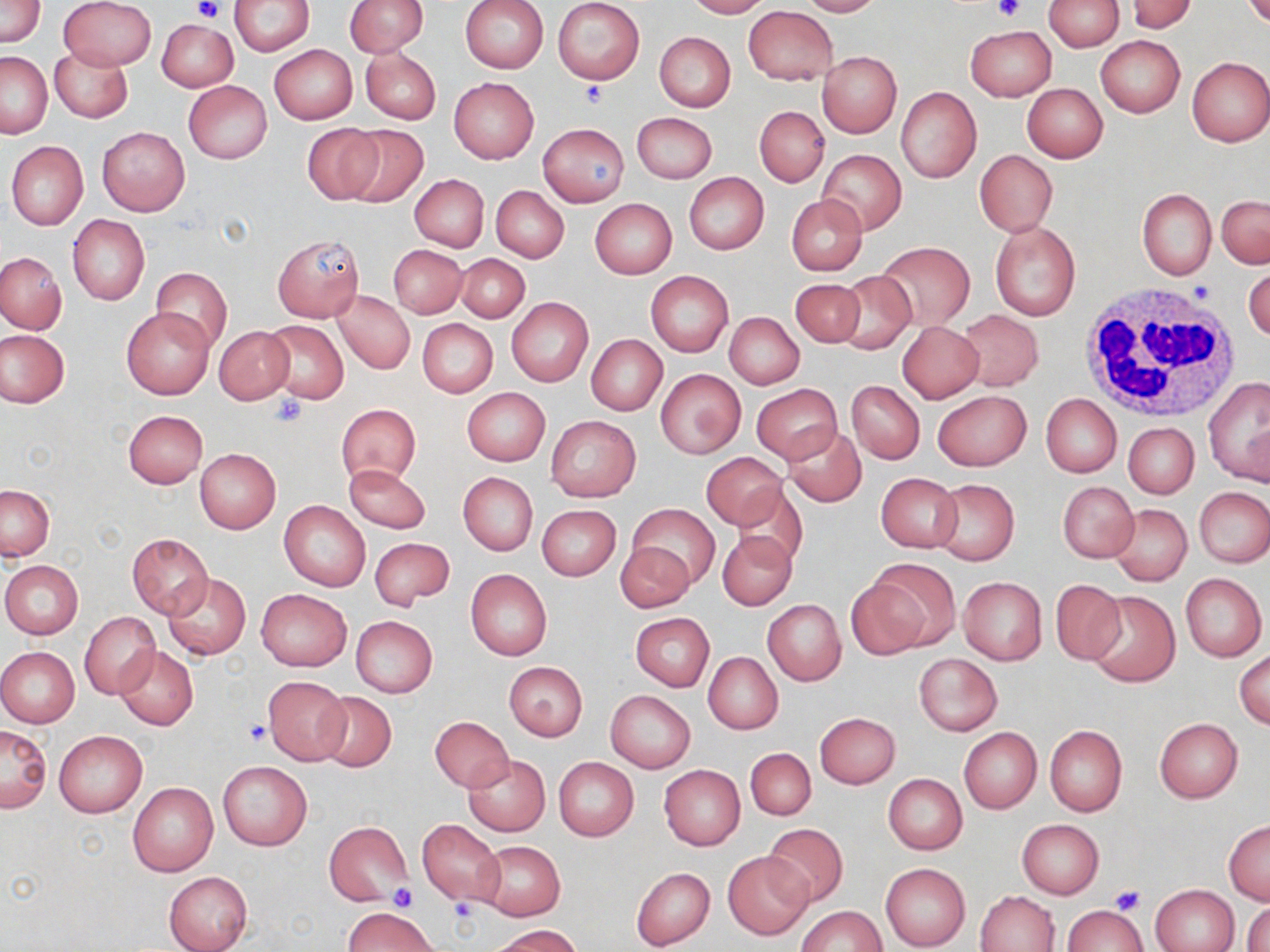
slide_level_diagnosis: negative for blood parasites
field_of_view: one of a larger specimen
uninfected_red_blood_cell_locations: 'approximate bounding boxes as [x1, y1, x2, y2] in pixels: [0, 0, 45, 48], [61, 0, 155, 69], [229, 0, 316, 56], [345, 0, 428, 56], [459, 0, 548, 73], [553, 0, 645, 84], [685, 0, 769, 18], [795, 0, 881, 17], [1043, 0, 1124, 50], [1126, 0, 1197, 34], [1244, 0, 1270, 29], [744, 6, 837, 85], [156, 18, 238, 92], [965, 26, 1056, 100], [653, 32, 735, 112], [1096, 36, 1184, 117], [640, 38, 719, 184], [270, 45, 357, 124], [51, 47, 133, 123], [360, 48, 440, 123], [818, 51, 901, 137], [1, 52, 51, 138], [1186, 57, 1270, 147], [449, 77, 539, 164], [183, 81, 271, 164], [1022, 83, 1108, 162], [896, 86, 982, 183], [755, 106, 828, 187], [632, 112, 716, 184], [301, 123, 386, 203], [340, 123, 429, 208], [537, 123, 630, 206], [98, 126, 190, 216], [6, 141, 89, 230], [817, 150, 906, 233], [974, 150, 1057, 237], [684, 173, 769, 255], [409, 174, 488, 253], [491, 186, 568, 263], [1137, 189, 1216, 279], [786, 194, 867, 276], [1216, 195, 1269, 269], [591, 199, 677, 279], [67, 215, 149, 305], [990, 221, 1080, 321], [273, 233, 363, 323], [876, 242, 975, 330], [388, 244, 467, 317], [0, 251, 66, 334], [455, 253, 530, 322], [1244, 265, 1270, 342], [151, 268, 231, 348], [646, 272, 733, 356], [831, 272, 918, 354], [790, 279, 866, 347], [332, 290, 415, 375], [506, 297, 593, 387], [121, 306, 215, 400], [955, 309, 1043, 389], [725, 312, 804, 388], [416, 318, 497, 397], [263, 320, 349, 404], [897, 322, 983, 403], [214, 327, 294, 405], [1, 331, 68, 407], [585, 334, 667, 415], [656, 370, 745, 460], [1203, 376, 1270, 486], [847, 381, 924, 464], [752, 384, 841, 463], [462, 388, 549, 466], [933, 390, 1031, 471], [1041, 393, 1122, 477], [337, 403, 421, 485], [122, 409, 207, 488], [545, 416, 641, 502], [1123, 422, 1200, 499], [781, 425, 867, 509], [194, 448, 281, 533], [702, 453, 787, 530], [344, 465, 430, 533], [457, 472, 537, 555], [877, 473, 962, 551], [931, 480, 1019, 567], [1058, 482, 1139, 563], [733, 484, 808, 568], [1, 485, 54, 560], [1195, 486, 1269, 568], [279, 500, 370, 591], [626, 503, 721, 591], [1109, 503, 1192, 585], [536, 505, 620, 580], [717, 529, 798, 611], [126, 533, 213, 618], [370, 537, 455, 611], [616, 541, 695, 612], [1, 561, 83, 638], [862, 561, 959, 652], [464, 568, 552, 660], [161, 571, 252, 660], [1181, 573, 1267, 662], [958, 576, 1047, 665], [1051, 581, 1127, 665], [257, 589, 351, 672], [1083, 590, 1180, 688], [762, 599, 846, 685], [79, 612, 160, 699], [630, 612, 714, 692], [350, 616, 437, 698], [114, 645, 198, 731], [0, 647, 80, 728], [1235, 650, 1270, 728], [703, 652, 782, 734], [913, 653, 1001, 735], [504, 661, 587, 740], [262, 675, 351, 765], [605, 690, 696, 771], [315, 691, 397, 771], [815, 712, 900, 788], [430, 716, 515, 792], [1153, 718, 1243, 803], [1, 723, 52, 813], [1044, 724, 1127, 817], [958, 726, 1042, 814], [54, 729, 148, 817], [744, 748, 817, 821], [464, 755, 550, 836], [554, 757, 639, 841], [218, 761, 312, 850], [659, 764, 745, 850], [884, 774, 966, 854], [127, 782, 217, 876], [417, 819, 506, 906], [1224, 819, 1269, 904], [1016, 820, 1104, 898], [323, 821, 412, 904], [762, 823, 850, 907], [476, 839, 564, 920], [723, 849, 814, 940], [881, 863, 970, 950], [631, 867, 714, 950], [163, 872, 252, 952], [1151, 885, 1239, 952], [976, 890, 1061, 951], [1244, 901, 1269, 952], [1064, 904, 1147, 951], [795, 905, 886, 952], [344, 906, 438, 951], [493, 924, 583, 951]'
image_size: 1270×952 pixels
white_blood_cell_locations: 'approximate bounding boxes as [x1, y1, x2, y2] in pixels: [1078, 286, 1246, 424]'
magnification: 1000x
platelet_locations: 'approximate bounding boxes as [x1, y1, x2, y2] in pixels: [192, 0, 222, 21], [994, 0, 1026, 23], [578, 79, 609, 107], [271, 393, 309, 428], [244, 720, 271, 746], [388, 885, 418, 912], [1109, 886, 1143, 914], [449, 891, 479, 924]'
preparation: thin blood film
modality: optical microscopy
stain: May-Grünwald-Giemsa